Comment on the morphology of the erythrocytes.
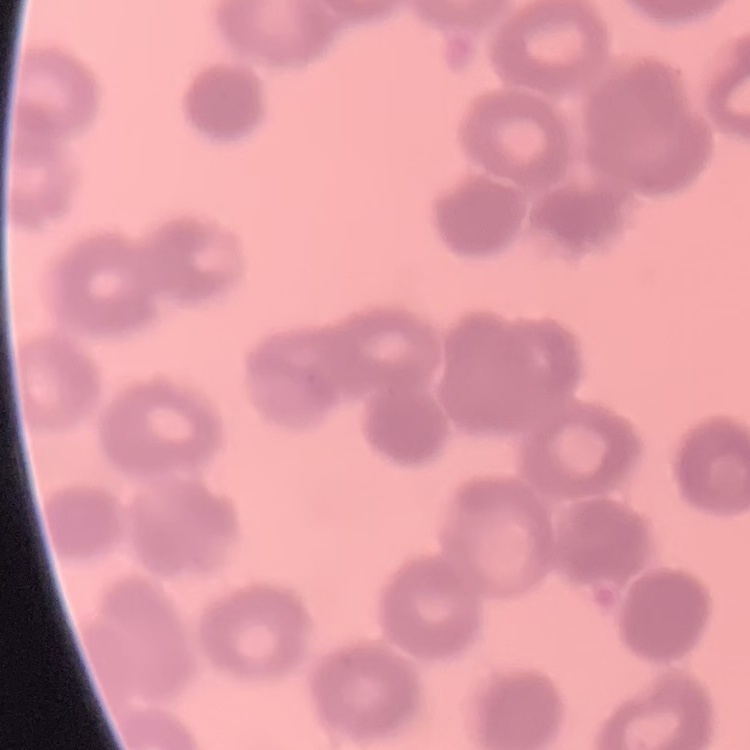

Rouleaux formation.

Summary:
  - Preparation: thin peripheral smear
  - Image type: square crop of a larger photomicrograph
  - Stain: Field's or Giemsa